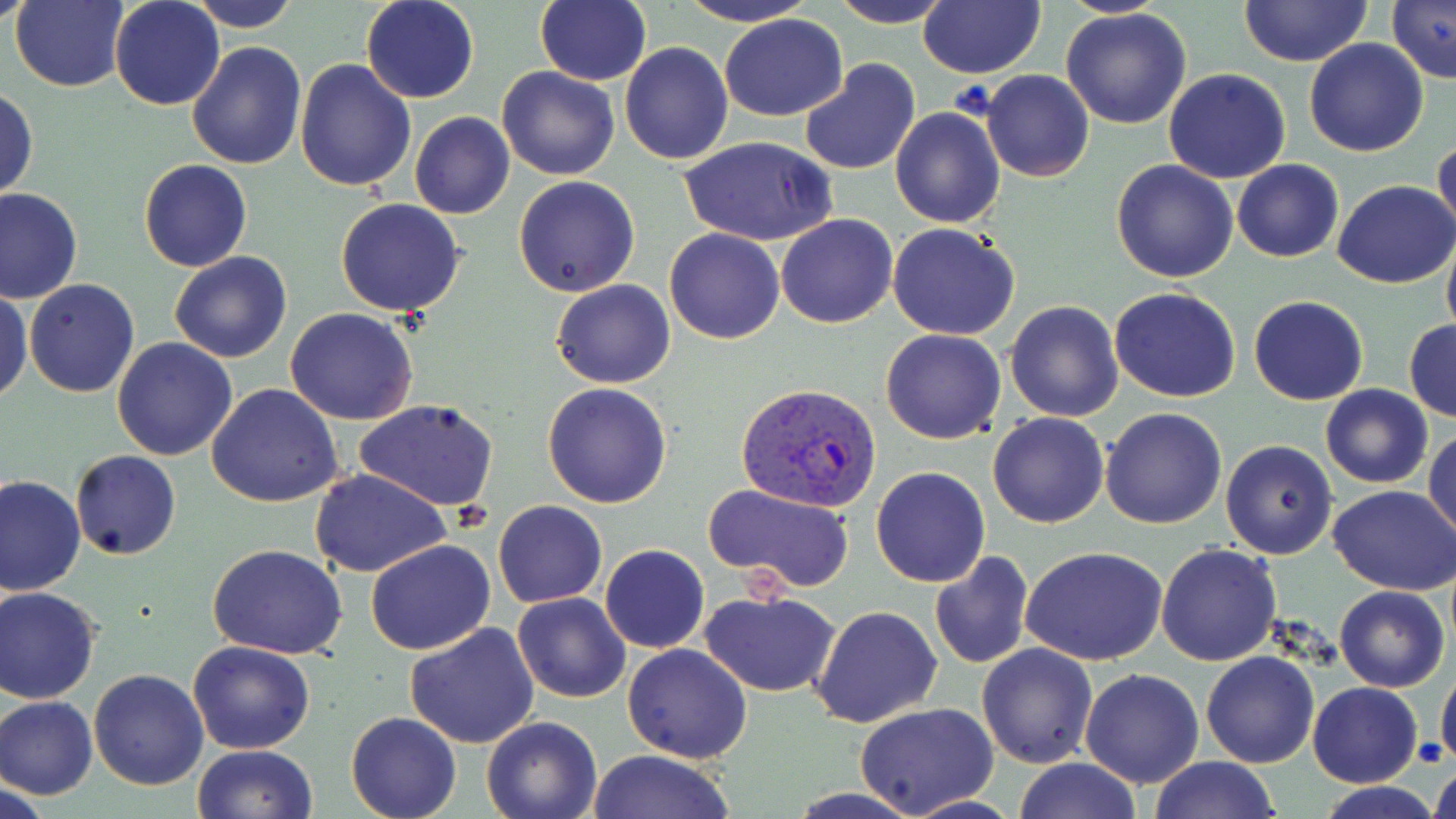
Approximate bounding boxes as [x1, y1, x2, y2] in pixels. Plasmodium vivax-infected red blood cell locations: [739, 384, 881, 512]. Uninfected red blood cell locations: [0, 0, 40, 30], [11, 0, 129, 91], [109, 0, 226, 110], [188, 0, 302, 32], [360, 0, 480, 104], [536, 0, 651, 85], [674, 0, 822, 27], [830, 0, 951, 28], [917, 0, 1045, 79], [1385, 0, 1454, 87], [1055, 1, 1178, 18], [1240, 1, 1373, 67], [1060, 7, 1193, 129], [720, 14, 848, 122], [1304, 36, 1430, 158], [619, 41, 733, 165], [186, 42, 308, 170], [295, 59, 418, 192], [798, 59, 921, 176], [496, 65, 619, 181], [1163, 68, 1292, 183], [980, 70, 1095, 182], [1, 86, 37, 202], [891, 106, 1006, 228], [410, 112, 514, 219], [679, 134, 835, 246], [1432, 135, 1456, 248], [1110, 158, 1237, 282], [139, 159, 252, 272], [1231, 159, 1343, 261], [513, 175, 641, 297], [1332, 179, 1455, 287], [1, 187, 83, 303], [335, 198, 467, 317], [775, 214, 899, 328], [887, 222, 1020, 340], [664, 229, 786, 345], [1441, 235, 1456, 342], [169, 250, 292, 363], [551, 278, 675, 387], [24, 279, 140, 398], [1109, 287, 1241, 402], [0, 288, 30, 405], [1247, 296, 1369, 405], [1005, 301, 1123, 421], [285, 308, 419, 426], [1404, 320, 1456, 422], [879, 329, 1007, 445], [112, 337, 239, 460], [541, 382, 673, 508], [206, 383, 343, 507], [1320, 385, 1433, 488], [354, 399, 498, 510], [1100, 407, 1228, 529], [988, 412, 1110, 528], [1425, 429, 1456, 541], [1221, 439, 1339, 559], [69, 450, 181, 560], [870, 465, 992, 586], [311, 469, 452, 578], [0, 473, 86, 595], [703, 484, 855, 593], [1328, 485, 1456, 597], [493, 500, 607, 608], [365, 539, 496, 656], [1155, 542, 1282, 666], [600, 543, 709, 652], [208, 545, 349, 659], [1019, 545, 1168, 666], [930, 552, 1034, 670], [1334, 585, 1449, 692], [0, 586, 101, 704], [700, 589, 843, 695], [513, 592, 631, 703], [809, 605, 943, 728], [405, 621, 540, 749], [826, 635, 966, 794], [186, 640, 314, 755], [976, 642, 1100, 768], [622, 643, 752, 764], [1200, 650, 1321, 767], [1436, 663, 1456, 772], [89, 668, 209, 789], [1080, 669, 1203, 788], [1306, 681, 1422, 786], [0, 695, 99, 799], [856, 704, 999, 819], [346, 712, 461, 819], [480, 716, 601, 819], [191, 745, 316, 819], [585, 749, 736, 819], [1148, 756, 1280, 818], [1428, 757, 1456, 819], [1012, 758, 1141, 818], [2, 779, 54, 819], [1315, 781, 1442, 818]. Slide-level diagnosis: Plasmodium vivax. 1000x magnification. Light microscopy. Thin blood film. Image is 1456×819 pixels. One field of a larger specimen. May-Grünwald-Giemsa-stained preparation.